Evaluate for malaria.
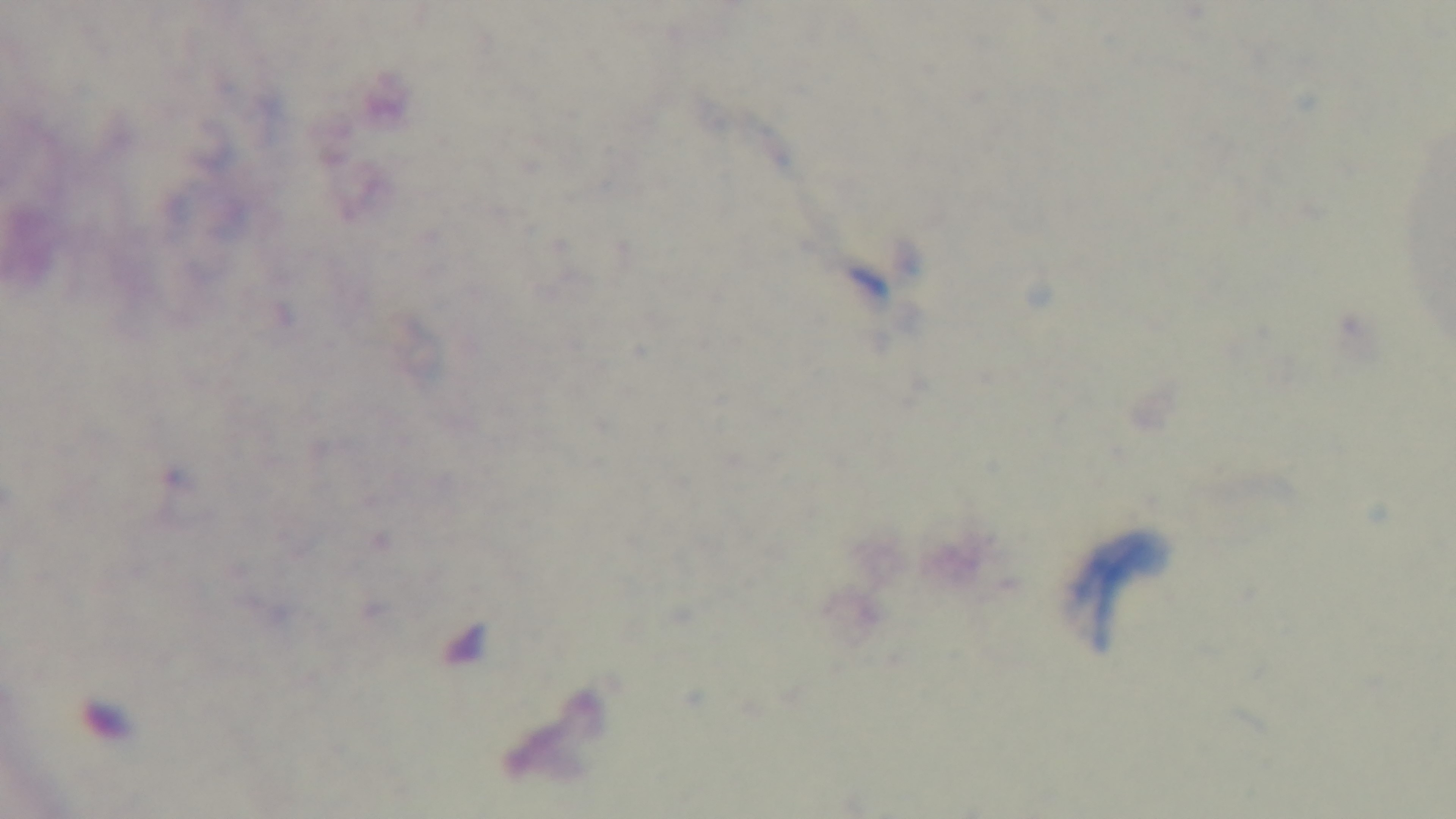

Uninfected.

Giemsa stain. Preparation: thick. Light microscopy. Captured with a mounted 4K digital camera. Single field of view. 100x oil-immersion objective.